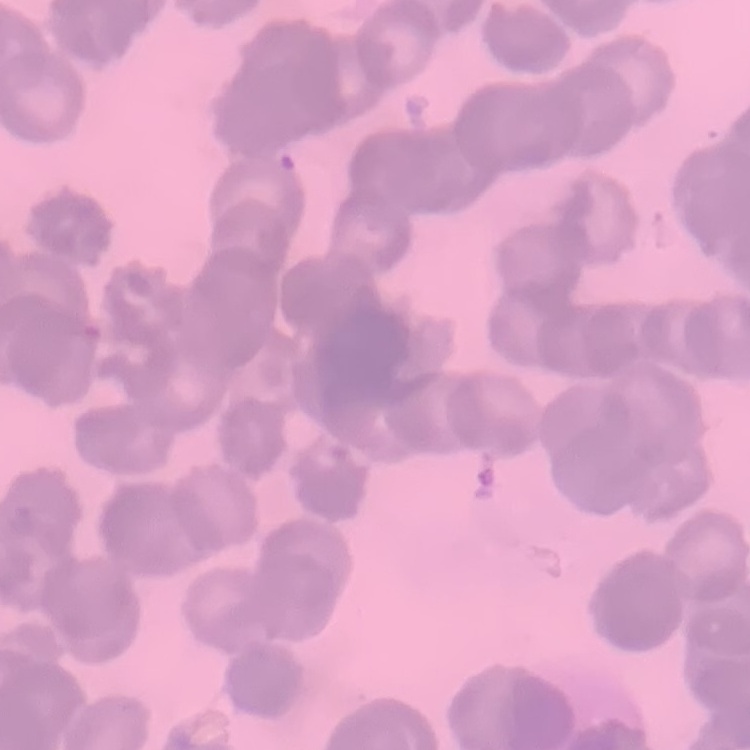
Summary:
  - Red blood cell morphology: rouleaux formation
  - Image type: square crop of a larger photomicrograph
  - Preparation: thin blood film
  - Stain: Field's or Giemsa